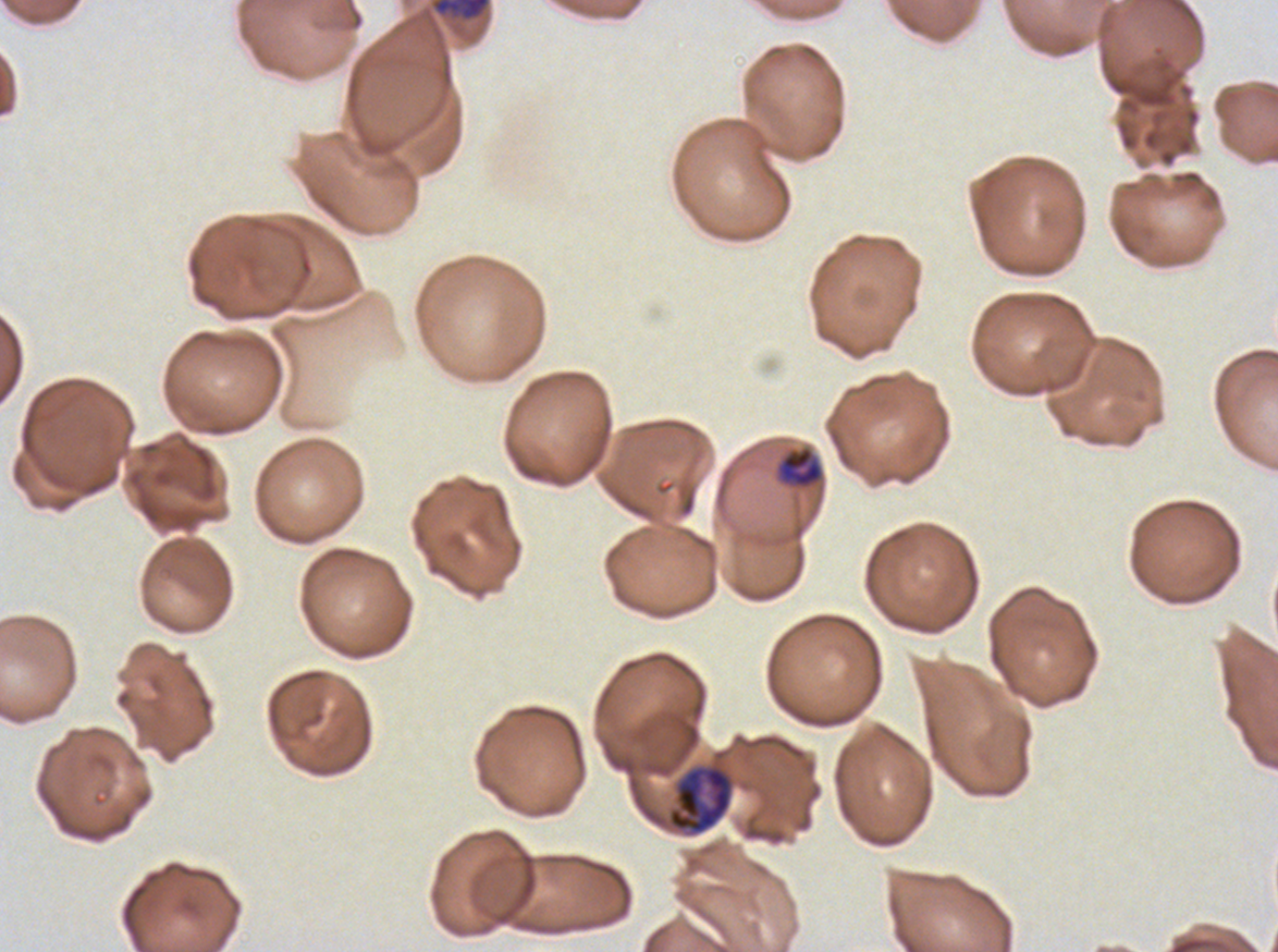 Approximate bounding rectangles given as corner coordinates in pixels from the top-left. Early schizont locations: (x1=432, y1=0, x2=491, y2=21). Late trophozoite locations: (x1=668, y1=765, x2=732, y2=834). Late-ring/early-trophozoite locations: (x1=778, y1=446, x2=823, y2=488). Thin blood film. Life-cycle stages observed: late-ring/early-trophozoite, late trophozoite, early schizont. Ex-vivo P. falciparum culture from a patient in The Gambia, grown for 24 to 48 hours. One sub-image of a larger composite. Giemsa stain. Image is 1278×952 pixels.